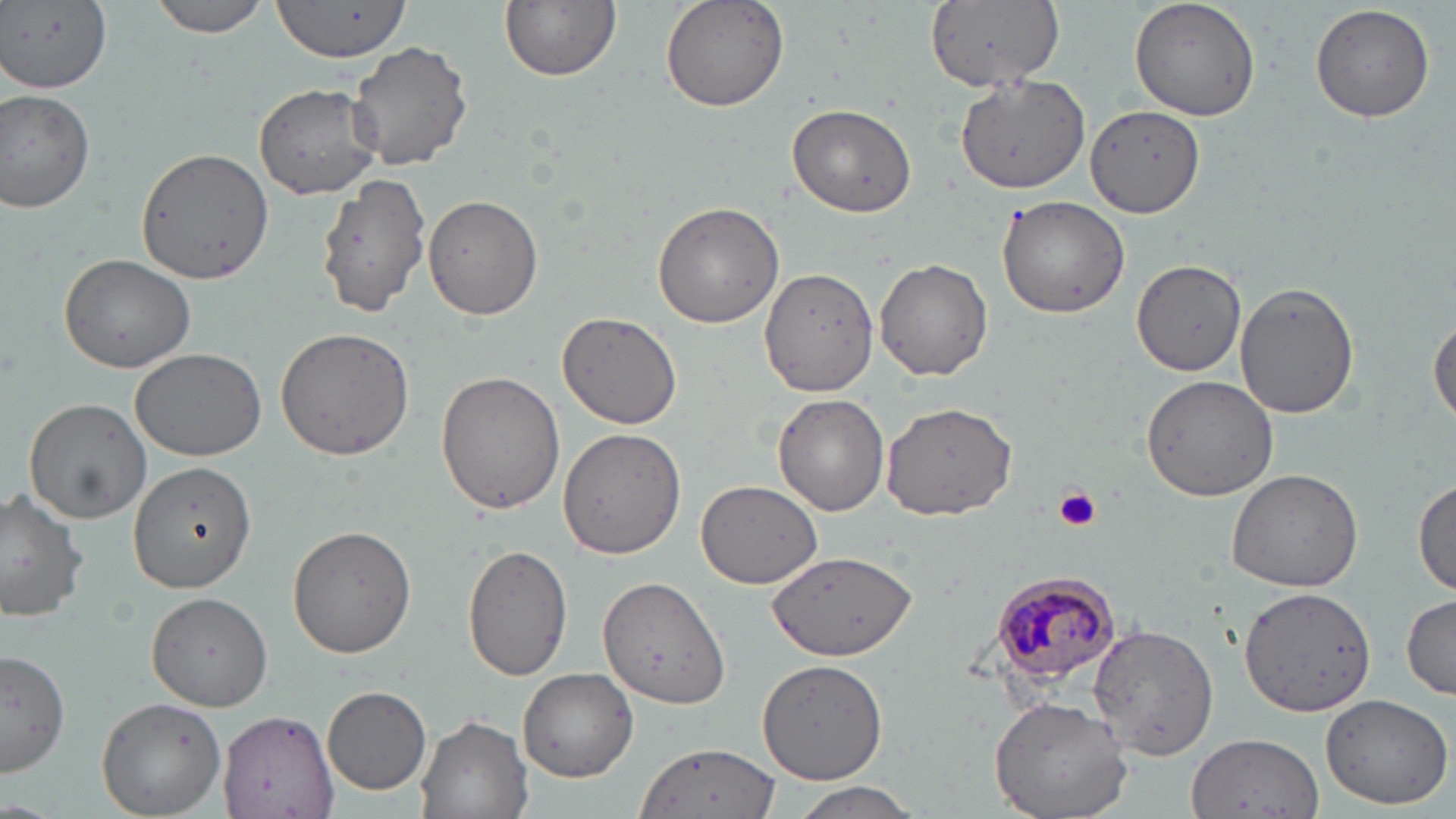
slide-level diagnosis = Plasmodium malariae
modality = light microscopy
Plasmodium malariae-infected red blood cell locations = approximate bounding boxes as (x1, y1, x2, y2) in pixels: (989, 568, 1125, 688)
preparation = thin blood film
platelet locations = approximate bounding boxes as (x1, y1, x2, y2) in pixels: (1053, 487, 1101, 533)
uninfected red blood cell locations = approximate bounding boxes as (x1, y1, x2, y2) in pixels: (4, 0, 113, 93), (500, 0, 621, 82), (659, 0, 789, 114), (926, 0, 1062, 98), (1130, 0, 1263, 121), (148, 1, 271, 38), (270, 2, 411, 62), (1310, 3, 1436, 123), (345, 38, 475, 175), (953, 72, 1094, 194), (253, 82, 381, 200), (0, 88, 96, 214), (787, 103, 917, 218), (1086, 104, 1206, 218), (134, 146, 277, 287), (313, 173, 433, 317), (422, 193, 543, 319), (996, 195, 1131, 319), (652, 202, 786, 329), (58, 252, 196, 374), (1133, 257, 1248, 377), (874, 258, 991, 382), (760, 266, 881, 398), (1236, 281, 1360, 418), (557, 312, 681, 429), (1429, 312, 1456, 429), (275, 327, 415, 463), (129, 347, 267, 460), (436, 369, 567, 512), (1140, 373, 1280, 503), (773, 395, 889, 516), (23, 397, 151, 524), (880, 401, 1018, 521), (557, 428, 686, 559), (127, 462, 255, 592), (1226, 467, 1365, 592), (1412, 475, 1456, 596), (694, 478, 824, 588), (0, 487, 93, 624), (288, 525, 417, 657), (462, 544, 574, 682), (769, 550, 915, 661), (596, 576, 729, 709), (1237, 584, 1376, 720), (147, 592, 274, 711), (1402, 594, 1456, 699), (1084, 616, 1223, 760), (0, 646, 70, 777), (758, 658, 886, 784), (518, 668, 637, 782), (322, 687, 431, 794), (1319, 693, 1453, 809), (96, 696, 226, 818), (988, 696, 1134, 819), (219, 708, 337, 819), (416, 714, 532, 818), (1189, 730, 1323, 817), (633, 743, 782, 819), (785, 780, 928, 819)
image size = 1456×819 pixels
stain = May-Grünwald-Giemsa
field of view = single
magnification = 1000x